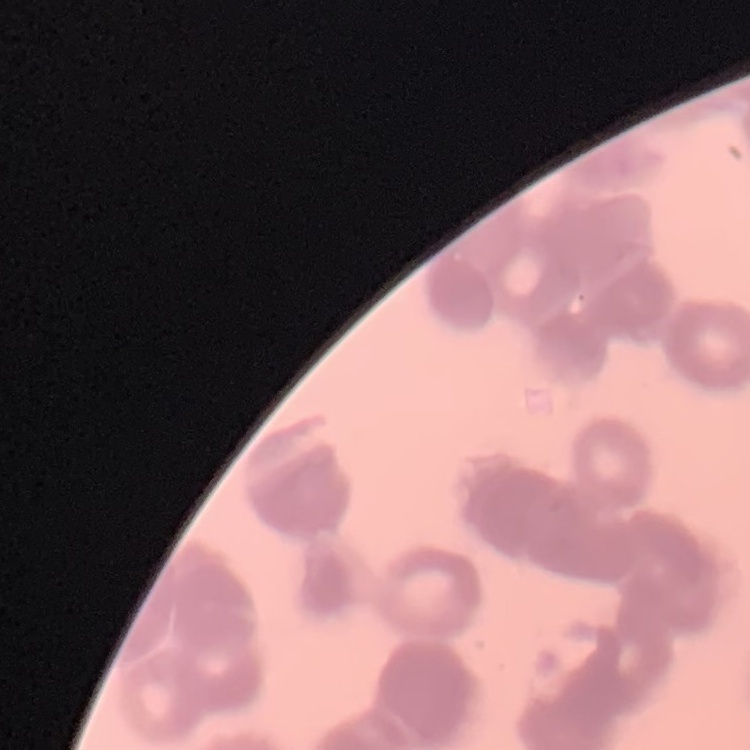

Summary:
  - Erythrocyte morphology: rouleaux formation
  - Preparation: thin blood smear
  - Stain: Field's or Giemsa
  - Image type: square crop of a larger photomicrograph